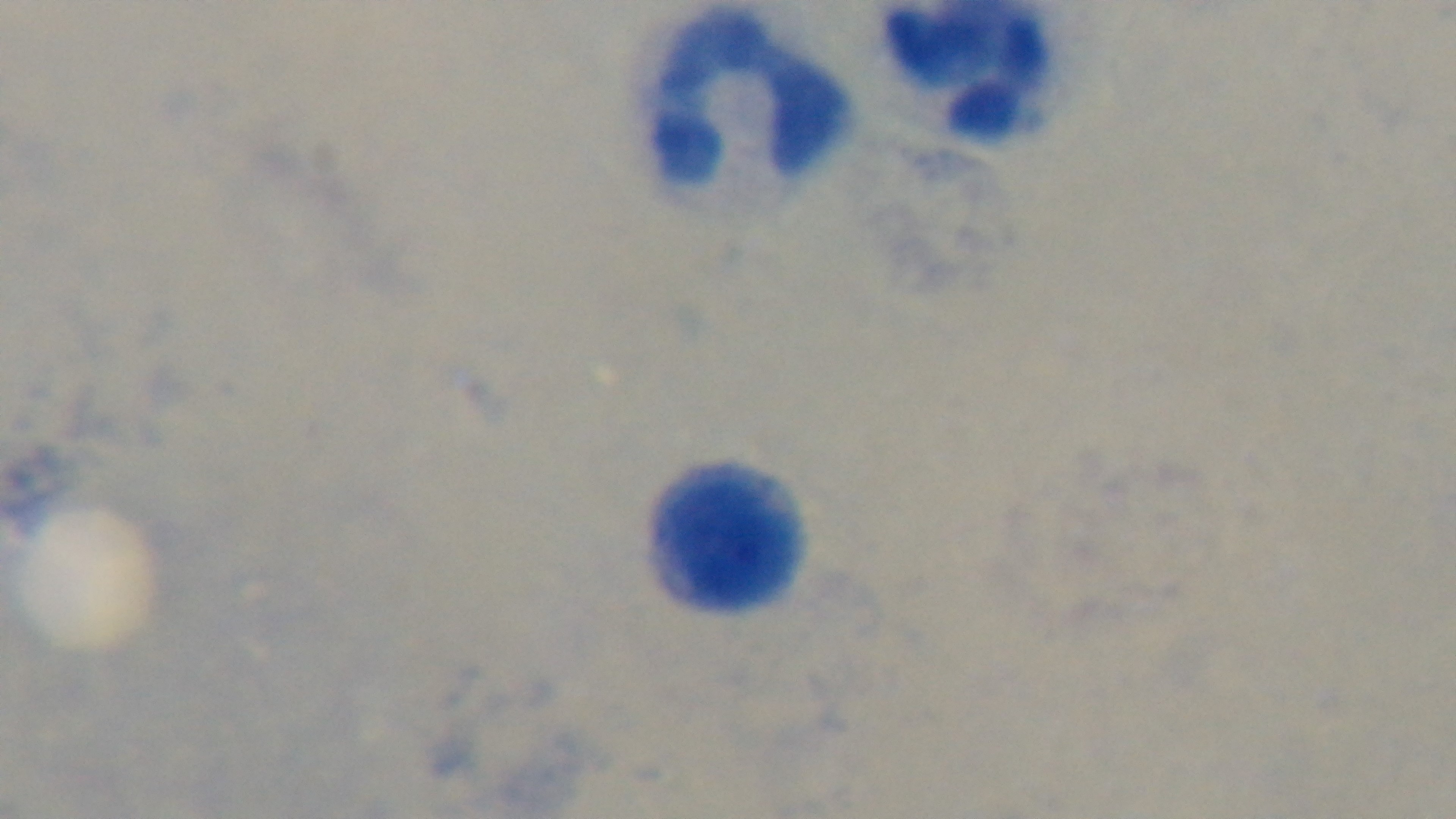

Summary:
  - Preparation: thick
  - Malaria status: negative
  - Stain: Giemsa
  - Modality: light microscopy
  - Objective: 100x oil immersion
  - Capture: mounted 4K digital camera
  - Field of view: one from the slide